Identify the parasite.
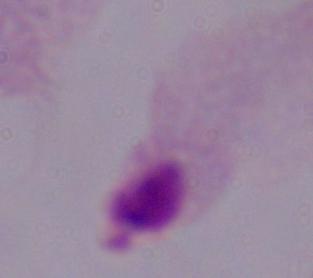

This is a trichomonad.

Summary:
  - Modality: micrograph
  - Magnification: 1000x